Assess this cell for malaria.
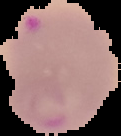

Parasitized.

Summary:
  - Preparation: thin blood film
  - Image type: segmented cell region with the area outside set to black
  - Image size: 121×136 pixels